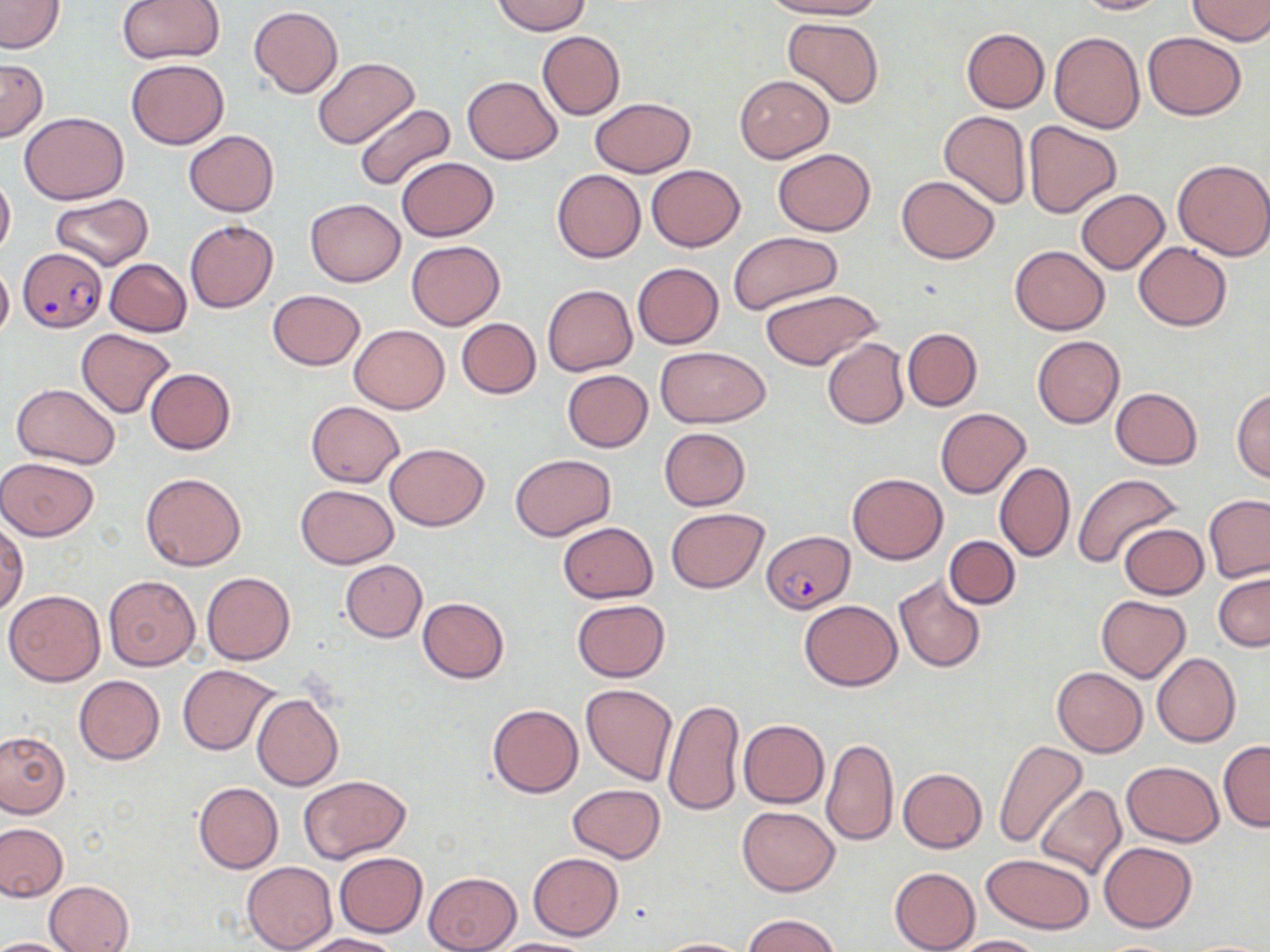
Approximate bounding boxes as (x1,y1)-(x2,y2) corner pairs in pixels. Plasmodium falciparum-infected red blood cell locations: (17,247)-(107,332), (763,529)-(853,612). Uninfected red blood cell locations: (116,0)-(223,64), (492,0)-(589,35), (759,0)-(881,20), (1071,0)-(1170,16), (1187,0)-(1270,43), (0,1)-(65,53), (249,6)-(343,97), (782,16)-(885,108), (960,28)-(1049,112), (536,31)-(625,120), (1049,31)-(1144,133), (1143,32)-(1245,119), (0,57)-(47,142), (313,57)-(420,150), (126,59)-(230,150), (734,74)-(834,163), (462,76)-(563,164), (590,97)-(695,177), (354,103)-(455,191), (939,111)-(1031,208), (19,112)-(129,203), (1022,119)-(1122,218), (183,130)-(279,216), (773,149)-(876,235), (396,157)-(499,241), (1173,158)-(1270,261), (647,165)-(744,250), (551,169)-(646,263), (0,174)-(16,257), (896,176)-(999,262), (1075,188)-(1169,275), (50,193)-(153,271), (305,199)-(405,286), (184,220)-(278,312), (729,232)-(843,316), (406,240)-(505,329), (1132,242)-(1233,331), (1009,245)-(1110,334), (105,259)-(191,336), (632,263)-(724,348), (0,264)-(13,340), (542,284)-(637,375), (759,288)-(883,372), (268,289)-(365,370), (456,318)-(541,398), (349,324)-(449,414), (902,328)-(982,411), (76,329)-(176,418), (1033,337)-(1125,428), (821,338)-(910,430), (657,346)-(769,427), (146,368)-(236,454), (562,370)-(652,452), (11,382)-(121,469), (1110,387)-(1203,470), (1232,388)-(1270,482), (306,401)-(403,487), (935,408)-(1030,498), (658,427)-(751,510), (384,442)-(489,531), (510,454)-(617,541), (0,457)-(101,540), (994,461)-(1075,562), (140,471)-(246,571), (847,472)-(947,564), (1073,473)-(1183,569), (295,485)-(400,569), (1204,494)-(1269,582), (665,508)-(770,593), (0,519)-(28,615), (557,521)-(658,604), (1118,524)-(1207,599), (944,536)-(1019,609), (340,560)-(427,642), (1214,571)-(1270,652), (202,572)-(296,665), (892,575)-(987,673), (104,576)-(201,671), (5,590)-(106,686), (1096,594)-(1191,682), (418,597)-(509,682), (572,599)-(671,682), (799,599)-(902,691), (1152,653)-(1241,748), (178,664)-(280,754), (1051,667)-(1147,757), (74,675)-(165,764), (580,683)-(678,785), (251,694)-(344,790), (663,699)-(744,816), (487,704)-(583,797), (739,719)-(829,808), (0,731)-(68,818), (822,736)-(898,847), (993,740)-(1087,848), (1219,741)-(1270,832), (1121,761)-(1225,846), (898,767)-(987,853), (297,774)-(412,864), (193,782)-(283,873), (568,784)-(666,862), (1037,785)-(1127,881), (737,805)-(839,895), (0,822)-(67,901), (1099,842)-(1196,931), (334,851)-(427,936), (528,852)-(623,940), (981,853)-(1094,935), (241,861)-(336,952), (889,865)-(1087,945), (889,866)-(981,951), (423,872)-(521,952), (43,880)-(134,951), (741,914)-(842,952), (302,933)-(402,952), (946,934)-(1043,951), (0,936)-(75,951), (484,938)-(594,952), (652,938)-(753,952). Slide-level diagnosis: Plasmodium falciparum. 1000x magnification. Image is 1270×952 pixels. May-Grünwald-Giemsa-stained preparation. One field of a larger specimen. Light microscopy. Thin blood smear.